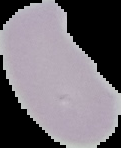 Malaria status: uninfected. The area outside the segmented cell region is set to black. Image is 121×148 pixels. From a thin blood film.